Assess the morphology of the erythrocytes.
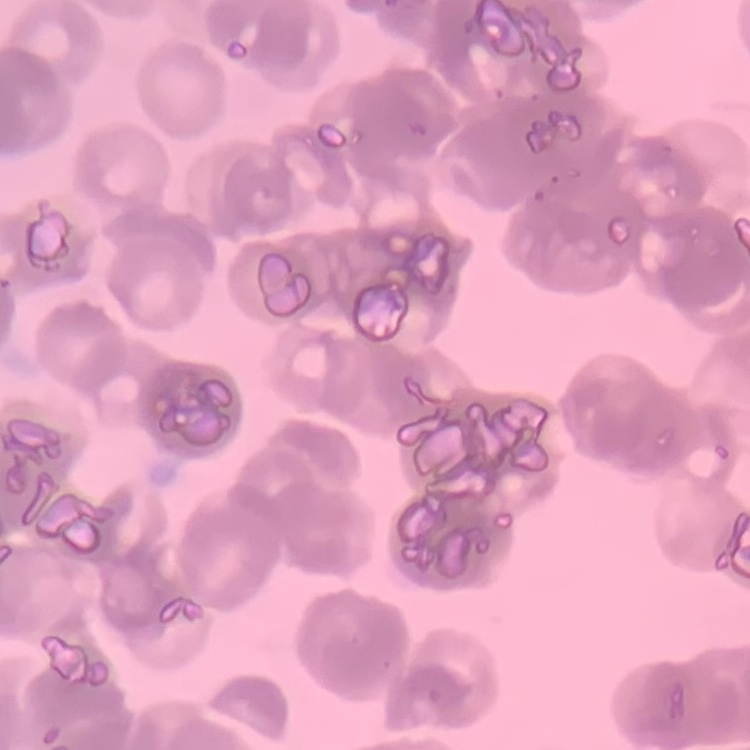

They show rouleaux formation.

Summary:
  - Image type: one tile cut from a larger photomicrograph
  - Preparation: thin peripheral smear
  - Stain: Field's or Giemsa